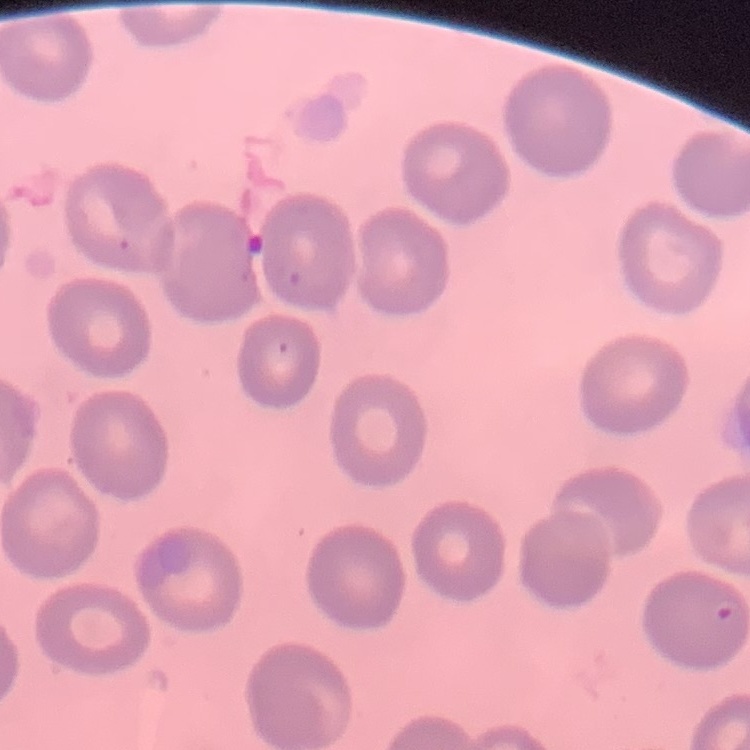

The red blood cells show no rouleaux formation. Thin blood film. Stained with either Field's or Giemsa. One tile cut from a larger photomicrograph.